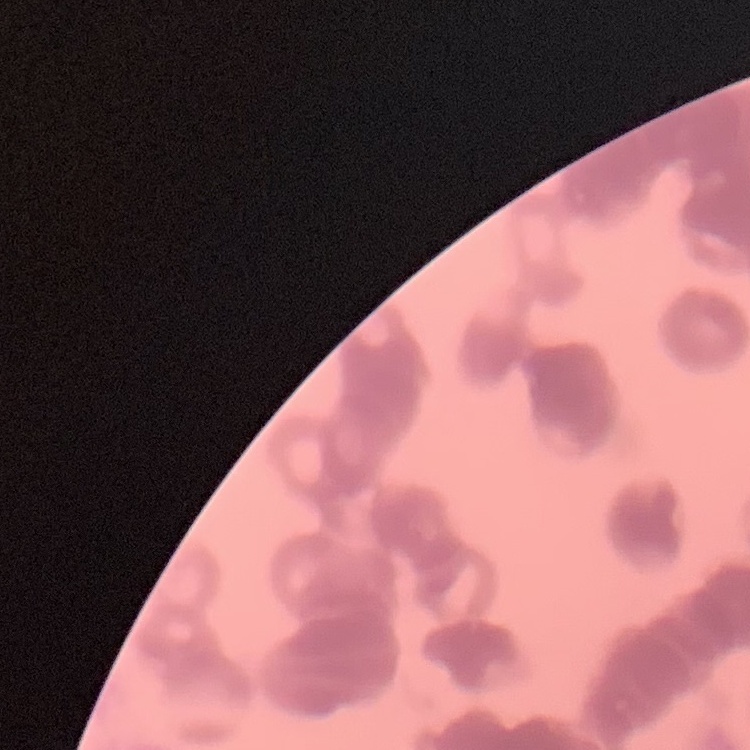

Summary:
  - Red blood cell morphology: rouleaux formation
  - Image type: one tile cut from a larger photomicrograph
  - Stain: Field's or Giemsa
  - Preparation: thin blood film